Assess this cell for malaria.
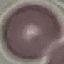

Uninfected.

Cell patch, automatically extracted from a larger field of view and resized to 64 × 64 pixels. Thin blood film. Photographed with a smartphone camera at the microscope eyepiece. Giemsa-stained preparation.